Describe the morphology of the red blood cells.
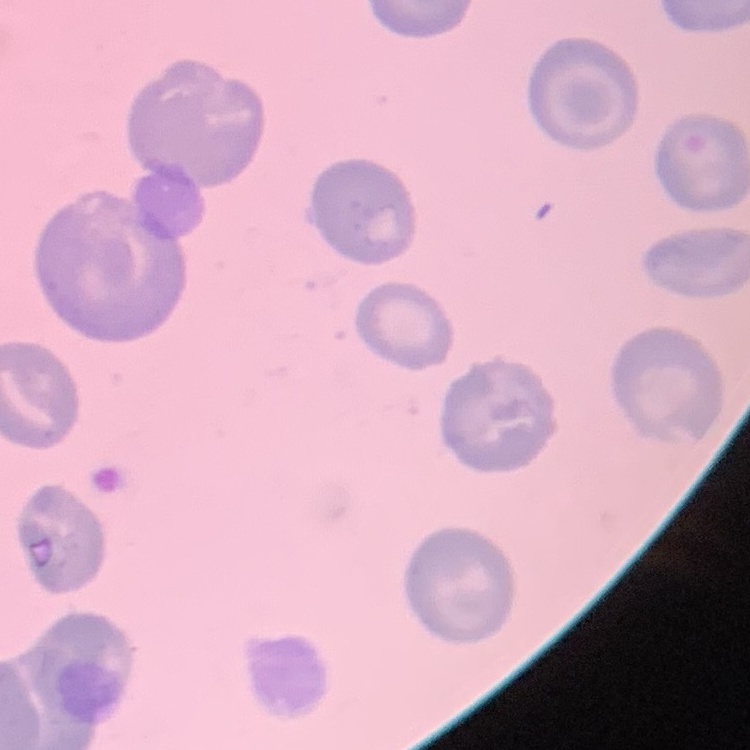
No rouleaux formation.

Summary:
  - Image type: square crop of a larger photomicrograph
  - Preparation: thin peripheral smear
  - Stain: Field's or Giemsa